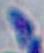
Summary:
  - Identification: Toxoplasma gondii
  - Magnification: 1000x
  - Modality: photomicrograph